Assess this cell for malaria.
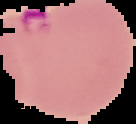
It is parasitized.

Cell region segmented out of the field of view; the surrounding area is masked to black. Image is 136×124 pixels. From a thin blood smear.